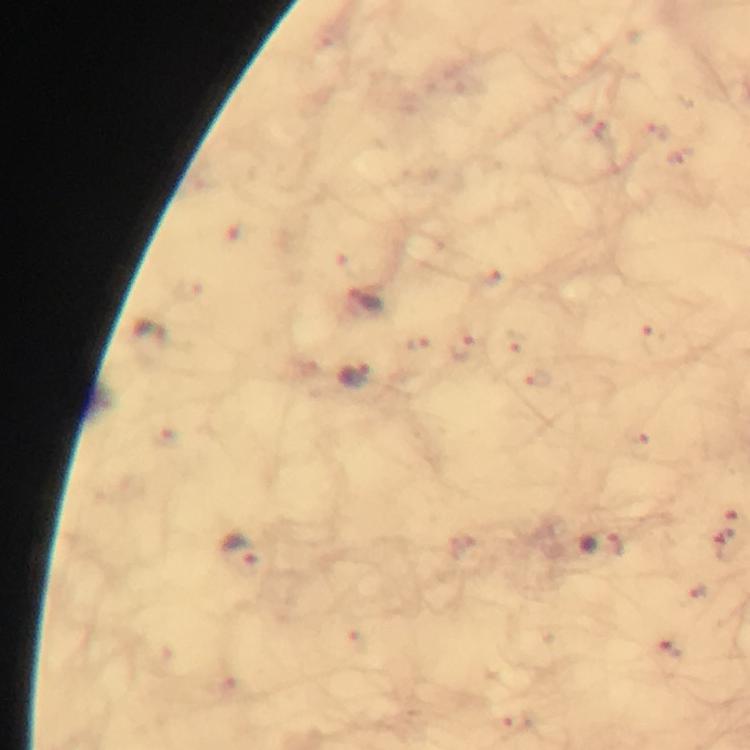

{
  "immersion_oil": "applied",
  "malaria_parasite_locations": "approximate centers as (x, y) in pixels: (654, 127), (601, 133), (497, 287), (366, 299), (150, 340), (654, 341), (464, 343), (511, 343), (352, 375), (540, 376), (636, 436), (727, 530), (601, 544), (239, 550), (697, 590), (671, 650), (515, 719)",
  "cropped_from": "one field of view",
  "stain": "Giemsa",
  "image_size": "750×750 pixels",
  "magnification": "100x",
  "preparation": "thick blood smear",
  "context": "from a malaria diagnostic workup",
  "capture": "smartphone camera through the microscope"
}